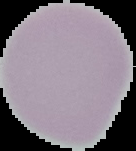

result = no Plasmodium parasites detected
image size = 136×151 pixels
preparation = thin blood film
image type = cell region segmented out of the field of view; surrounding area masked to black